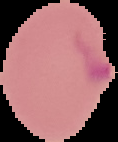

Segmented cell region on a black background. From a thin blood smear. Result: Plasmodium parasites detected. Image is 118×142 pixels.